Identify the parasite.
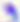
This is Toxoplasma gondii.

Summary:
  - Magnification: 400x
  - Modality: photomicrograph